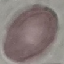

{
  "result": "no malaria parasites seen",
  "capture": "smartphone through the microscope eyepiece",
  "stain": "Giemsa",
  "image_type": "cell patch, automatically extracted from a larger field of view and resized to 64 × 64 pixels",
  "preparation": "thin blood film"
}